Identify the cell.
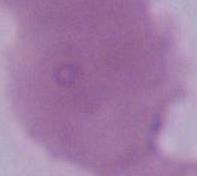
This is an erythrocyte.

magnification = 1000x
modality = micrograph